Give the position of every Plasmodium parasite, noting whether each is a trophozoite, schizont, or gametocyte.
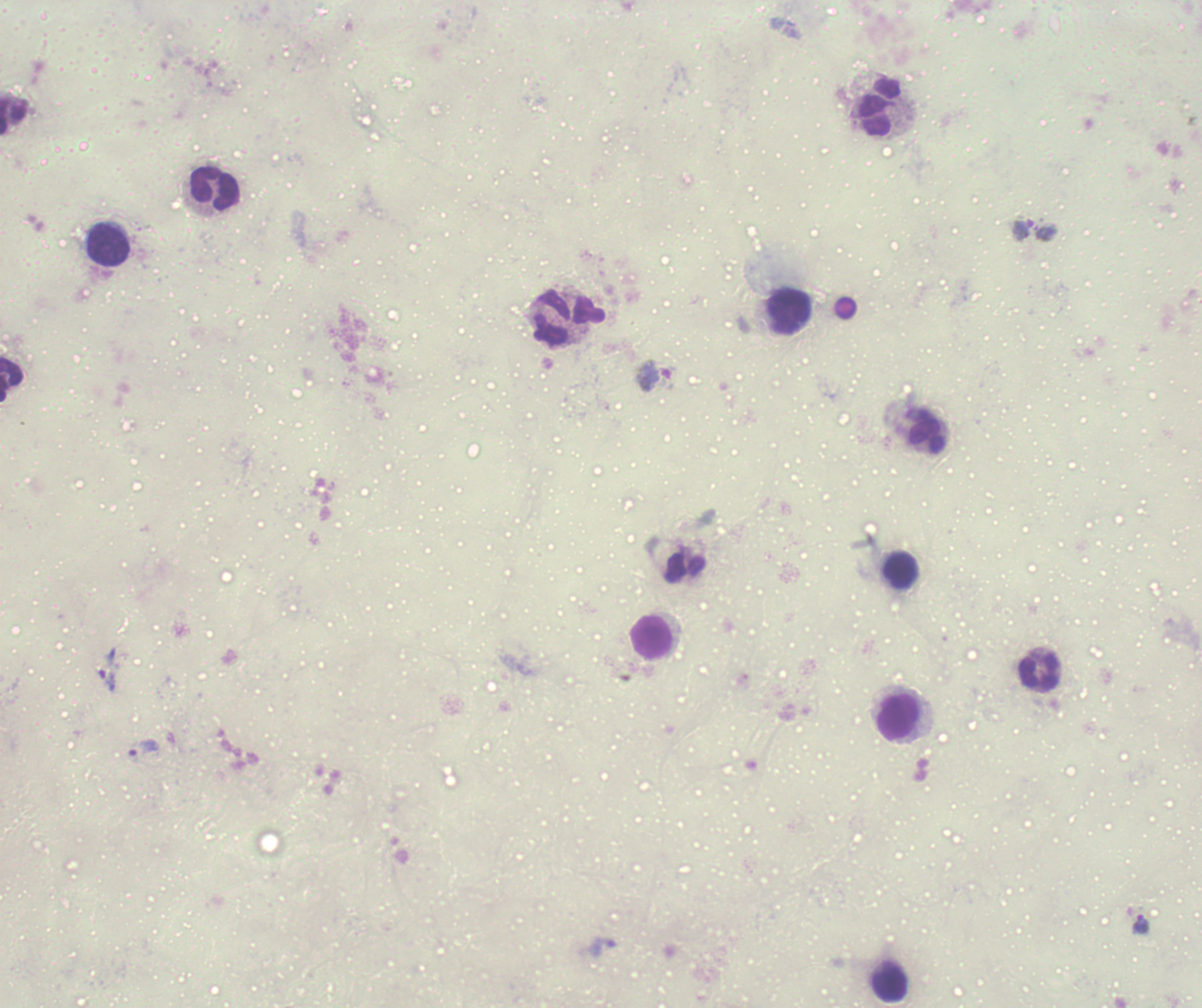

Approximate centers as [x, y] in pixels.
Trophozoites: [108, 670], [143, 748], [1140, 924].
Gametocytes: [1035, 229], [654, 376].
No schizont forms observed.

Approximate centers as [x, y] in pixels.
Summary:
  - Leukocyte locations: [879, 106], [14, 115], [215, 188], [108, 245], [790, 312], [552, 318], [11, 379], [927, 432], [900, 570], [652, 637], [1039, 671], [898, 718], [891, 984]
  - Coloration quality: bad
  - Image size: 1202×1008 pixels
  - Preparation: thick blood smear
  - Stain: Romanowsky
  - Magnification: 100x
  - Field of view: one from this slide
  - Context: previously used in an actual diagnosis
  - Background quality: unsatisfactory